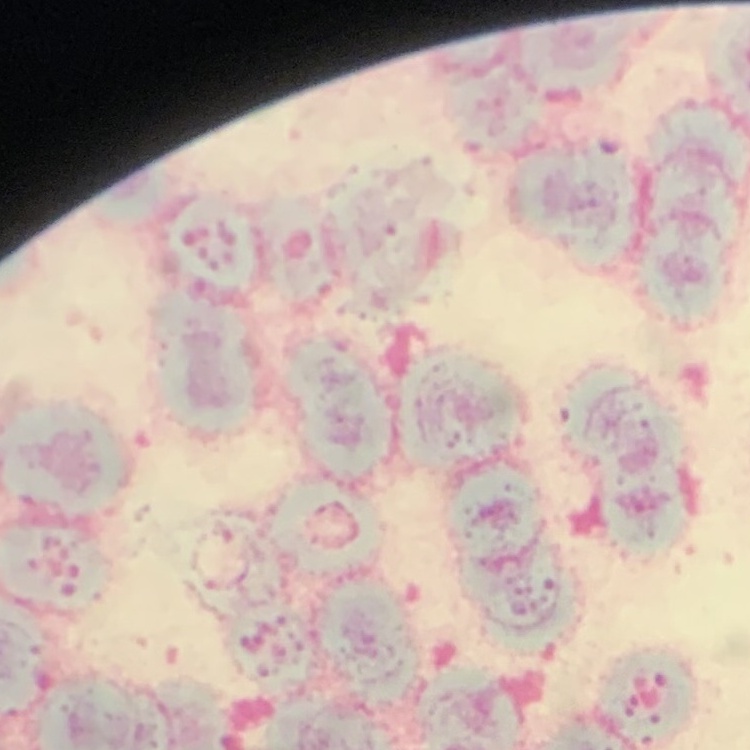
Summary:
  - Erythrocyte morphology: rouleaux formation
  - Preparation: thin blood smear
  - Stain: Field's or Giemsa
  - Image type: one tile cut from a larger photomicrograph